Classify this cell by malaria status.
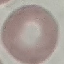
Uninfected.

image type = automatically extracted cell patch, resized to 64 × 64 pixels
capture = smartphone camera at the microscope eyepiece
stain = Giemsa
preparation = thin smear